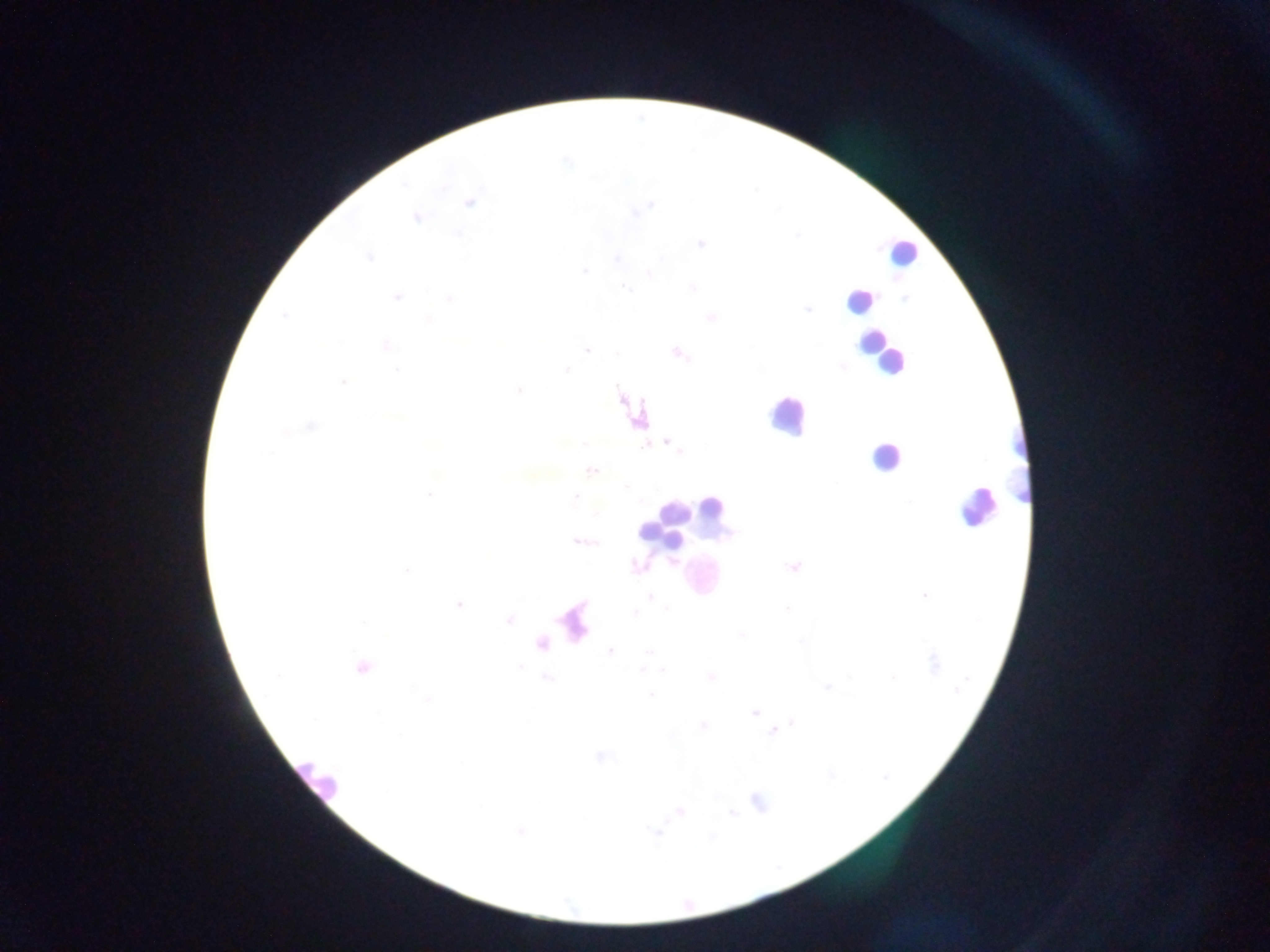
Approximate centers as [x, y] in pixels. Malaria parasite locations: [566, 161], [470, 202], [643, 207], [637, 212], [416, 217], [701, 243], [368, 257], [617, 258], [585, 270], [650, 274], [624, 288], [693, 288], [396, 297], [450, 298], [807, 310], [283, 316], [711, 318], [429, 320], [386, 346], [587, 350], [618, 353], [678, 353], [842, 366], [397, 371], [565, 371], [343, 382], [518, 389], [311, 426], [287, 431], [584, 444], [672, 445], [680, 451], [591, 470], [625, 485], [430, 494], [575, 498], [579, 541], [587, 543], [637, 567], [793, 567], [406, 570], [924, 595], [651, 597], [459, 605], [667, 608], [786, 609], [635, 613], [509, 619], [364, 621], [742, 635], [610, 652], [648, 653], [934, 662], [363, 667], [642, 670], [664, 670], [278, 675], [711, 676], [894, 677], [827, 687], [957, 691], [650, 695], [428, 699], [754, 713], [793, 722], [702, 726], [773, 730], [599, 756], [758, 801], [680, 811], [731, 813], [520, 831], [656, 833]. Leukocyte locations: [901, 252], [858, 301], [872, 345], [889, 361], [786, 415], [885, 457], [1018, 467], [712, 506], [975, 507], [669, 521], [652, 533], [670, 536], [700, 577], [317, 778]. One field of view. Photographed through a microscope with a mobile-phone camera. Image is 1270×952 pixels. Thick blood smear. Sample from Ghana.